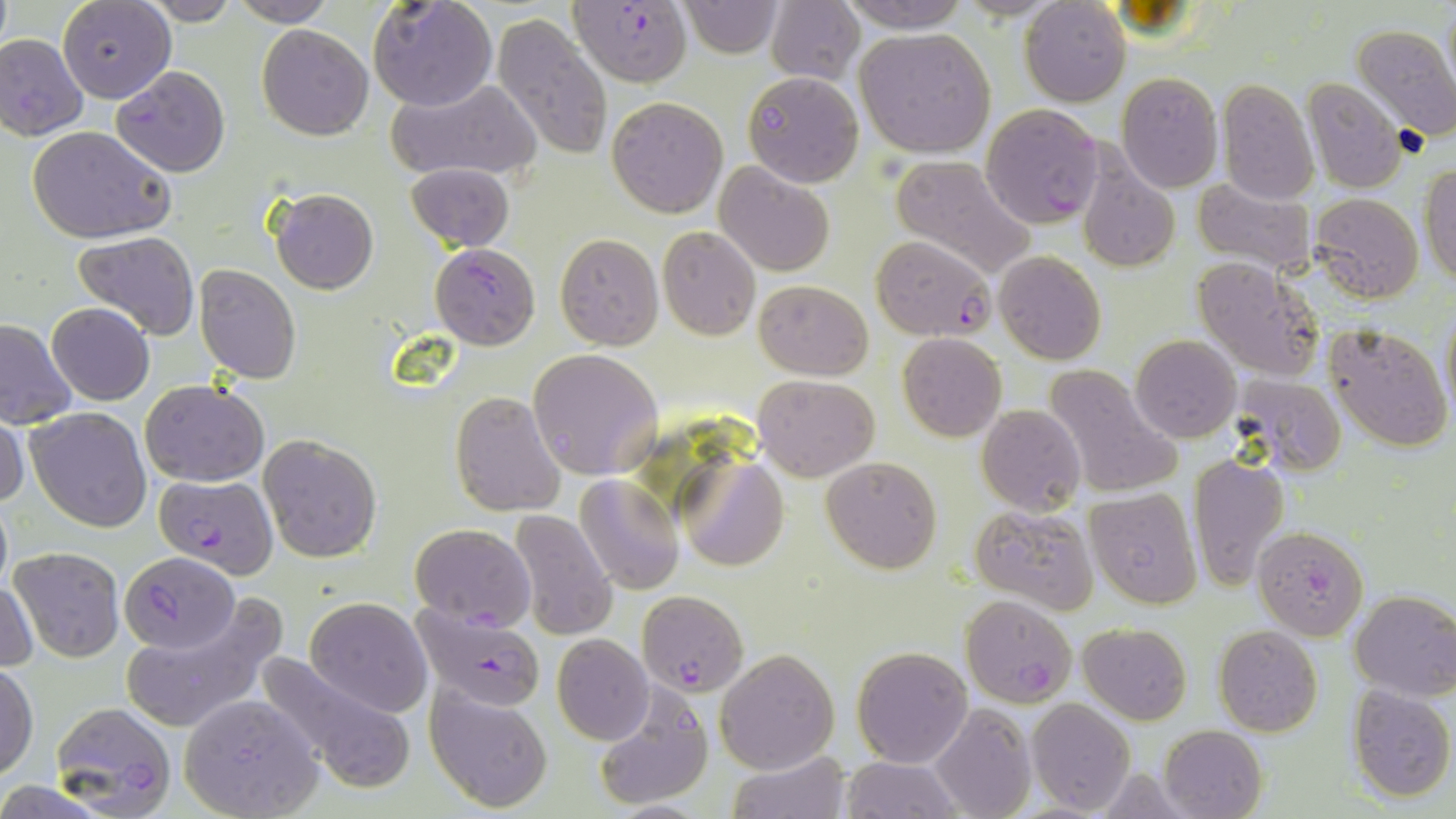

Approximate bounding boxes as (x1, y1, x2, y2) in pixels. Plasmodium falciparum-infected red blood cell locations: (569, 0, 692, 86), (0, 33, 89, 139), (113, 65, 231, 178), (982, 103, 1104, 229), (871, 235, 994, 340), (430, 243, 539, 349), (153, 472, 279, 578), (1254, 526, 1369, 640), (119, 551, 238, 653), (636, 589, 747, 697), (961, 594, 1077, 708), (412, 603, 550, 713), (50, 701, 178, 817). Uninfected red blood cell locations: (59, 0, 175, 102), (367, 0, 498, 112), (678, 0, 784, 57), (838, 0, 969, 31), (1020, 0, 1131, 106), (140, 1, 240, 25), (227, 1, 338, 26), (766, 2, 863, 84), (491, 14, 614, 162), (1350, 22, 1456, 140), (257, 24, 373, 140), (854, 26, 996, 158), (742, 71, 864, 188), (1116, 72, 1224, 193), (386, 77, 541, 181), (1304, 78, 1406, 193), (1218, 80, 1319, 204), (606, 96, 728, 219), (27, 127, 175, 243), (1073, 152, 1182, 275), (889, 155, 1037, 280), (405, 161, 514, 253), (715, 161, 835, 276), (1421, 163, 1455, 288), (1191, 178, 1317, 274), (270, 189, 378, 294), (1312, 193, 1422, 303), (657, 226, 761, 340), (73, 231, 200, 340), (555, 233, 662, 349), (994, 250, 1107, 364), (1194, 259, 1325, 383), (194, 264, 302, 384), (754, 279, 871, 379), (46, 302, 155, 406), (1440, 303, 1456, 417), (0, 316, 77, 428), (1325, 323, 1452, 451), (897, 333, 1006, 442), (1131, 334, 1241, 442), (527, 347, 661, 479), (1042, 364, 1180, 500), (754, 375, 879, 481), (1230, 377, 1345, 476), (140, 378, 269, 486), (450, 391, 565, 517), (976, 404, 1085, 515), (25, 406, 151, 533), (0, 410, 28, 513), (259, 434, 382, 562), (1189, 452, 1289, 591), (679, 456, 790, 572), (822, 456, 943, 574), (575, 475, 683, 593), (1084, 486, 1202, 609), (0, 491, 13, 598), (969, 503, 1098, 614), (509, 510, 618, 641), (410, 522, 535, 632), (10, 546, 125, 662), (2, 578, 38, 674), (1350, 590, 1456, 702), (118, 597, 284, 736), (305, 597, 432, 717), (1079, 622, 1191, 725), (1214, 625, 1324, 736), (553, 634, 654, 744), (852, 645, 973, 768), (714, 648, 838, 774), (253, 651, 419, 794), (0, 663, 37, 782), (424, 681, 553, 812), (589, 683, 713, 812), (1345, 685, 1456, 803), (177, 695, 322, 818), (1026, 699, 1135, 816), (929, 703, 1036, 819), (1159, 724, 1269, 819), (726, 750, 848, 819), (841, 756, 963, 817). Slide-level diagnosis: Plasmodium falciparum. One field of a larger specimen. May-Grünwald-Giemsa-stained preparation. Light microscopy. Captured at 1000x magnification. Thin blood film. Image is 1456×819 pixels.